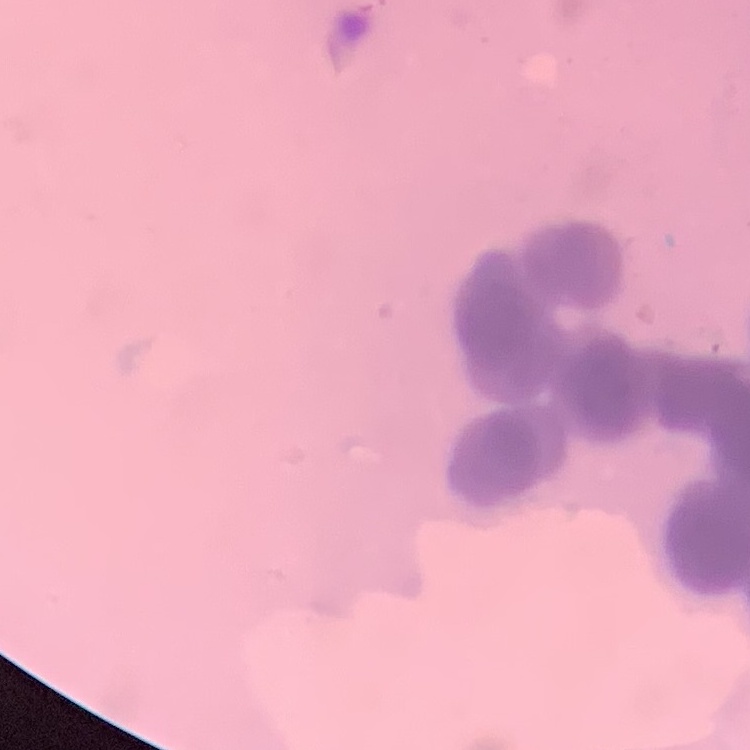

erythrocyte morphology = rouleaux formation
preparation = thin blood film
image type = square crop of a larger photomicrograph
stain = Field's or Giemsa